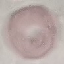

Summary:
  - Result: no malaria parasites seen
  - Capture: smartphone camera at the microscope eyepiece
  - Stain: Giemsa
  - Preparation: thin smear
  - Image type: cell patch, automatically extracted from a larger field of view and resized to 64 × 64 pixels